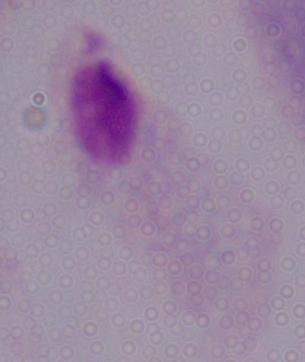
Summary:
  - Magnification: 1000x
  - Identification: trichomonad
  - Modality: photomicrograph